Point out each Plasmodium parasite.
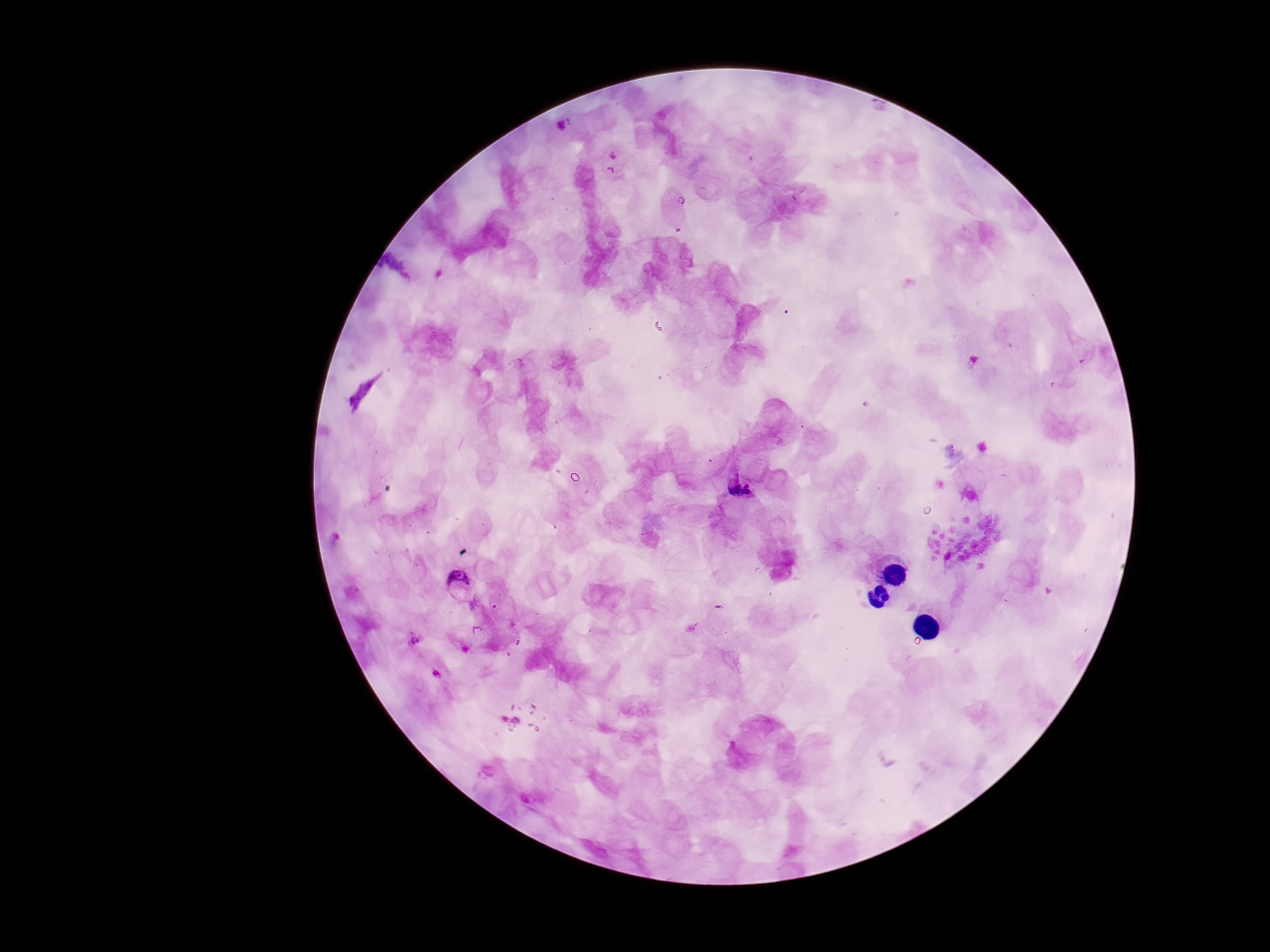
Approximate centers as (x, y) in pixels.
Plasmodium parasites: (563, 126), (682, 200), (738, 488), (458, 581), (414, 640).

field of view = one from this slide
capture = smartphone camera through the microscope eyepiece
image size = 1270×952 pixels
stain = Giemsa
magnification = 100x
preparation = thick blood smear
patient malaria status = infected